State the preparation type.
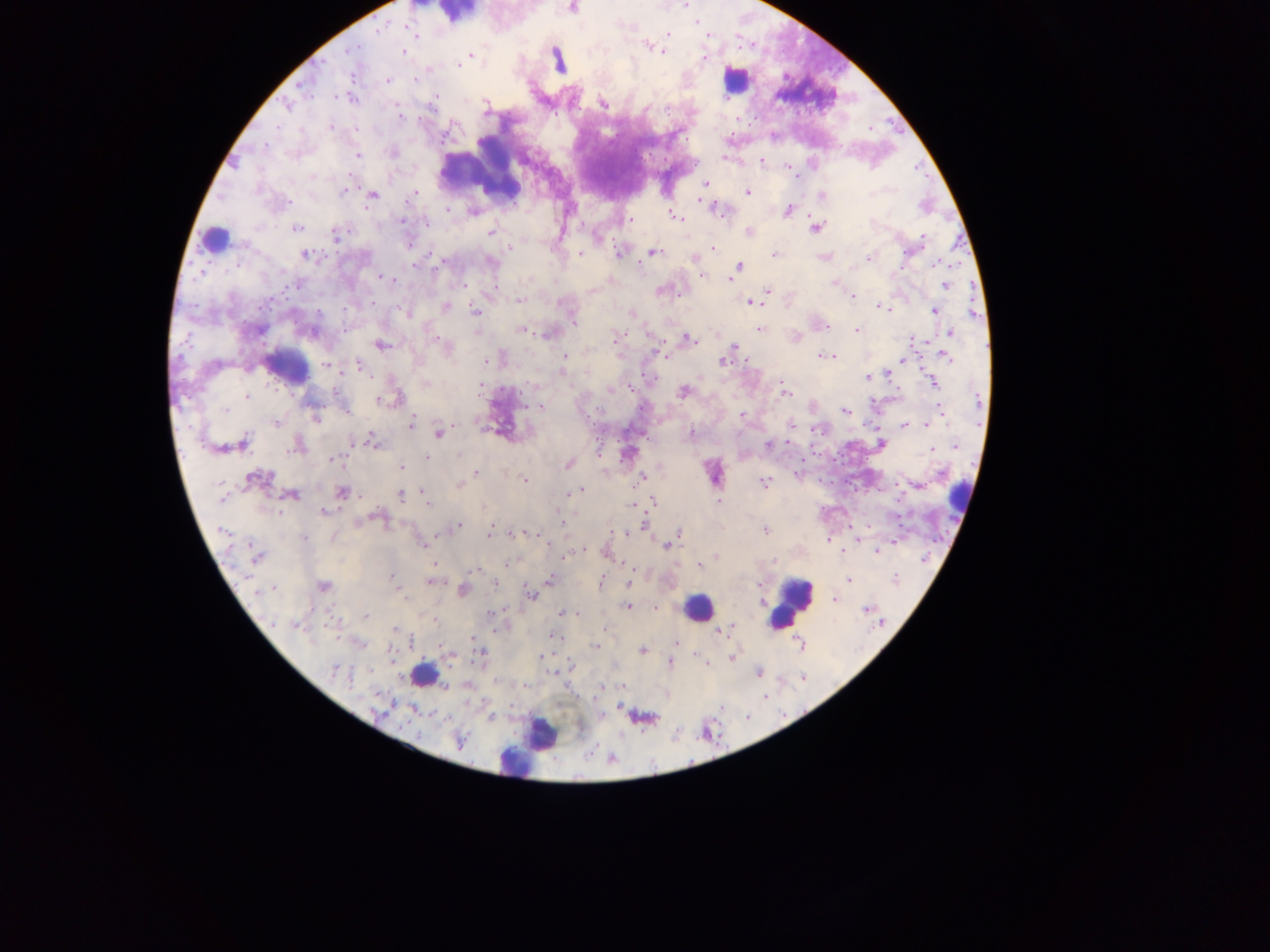

Thick blood film.

image size = 1270×952 pixels
field of view = single
malaria parasite locations = approximate centers as x y in pixels: 571 7; 667 34; 414 35; 708 36; 648 45; 347 50; 662 50; 402 51; 471 55; 703 58; 558 60; 457 65; 387 80; 413 81; 442 94; 602 103; 286 106; 486 106; 402 115; 556 116; 422 119; 330 127; 869 130; 734 132; 391 153; 357 155; 725 157; 759 161; 789 167; 912 169; 930 177; 705 184; 344 189; 747 192; 371 194; 413 195; 822 195; 700 202; 710 206; 715 208; 448 210; 788 210; 473 211; 677 216; 626 219; 401 220; 427 222; 815 226; 297 228; 491 232; 749 232; 336 236; 919 243; 713 248; 509 249; 620 252; 652 252; 580 253; 901 253; 305 255; 774 255; 869 256; 824 257; 694 258; 442 261; 490 262; 935 265; 415 266; 739 266; 901 268; 703 275; 381 278; 390 279; 730 280; 835 282; 292 285; 463 285; 944 285; 661 290; 767 290; 681 296; 852 296; 273 299; 519 301; 750 301; 194 306; 445 307; 879 307; 260 311; 475 312; 934 312; 407 313; 631 313; 573 322; 826 327; 520 329; 758 329; 856 329; 550 333; 950 333; 192 334; 433 337; 795 337; 615 338; 687 339; 924 341; 379 344; 734 346; 656 352; 565 354; 835 354; 832 355; 944 355; 823 356; 901 359; 487 360; 723 360; 746 360; 357 364; 327 365; 887 374; 867 376; 641 377; 783 382; 932 383; 426 384; 609 390; 522 391; 683 391; 783 392; 478 394; 394 397; 378 400; 539 406; 641 409; 846 411; 942 412; 589 415; 316 416; 742 416; 274 422; 410 423; 925 423; 905 425; 789 427; 815 429; 439 432; 692 433; 373 443; 240 444; 769 444; 880 444; 298 445; 956 445; 230 446; 931 449; 598 453; 628 453; 424 456; 839 457; 332 459; 801 459; 568 463; 401 467; 476 472; 797 474; 642 477; 817 478; 256 479; 524 480; 764 484; 836 484; 460 485; 917 485; 581 488; 341 491; 422 491; 290 494; 400 494; 569 494; 652 500; 427 502; 718 502; 633 504; 323 512; 378 517; 562 523; 645 523; 456 526; 869 527; 850 528; 765 530; 677 532; 515 533; 625 533; 487 535; 828 540; 895 541; 549 543; 423 544; 666 545; 876 550; 582 551; 843 551; 606 552; 257 556; 717 556; 562 558; 924 560; 773 561; 506 563; 700 565; 632 569; 473 571; 894 574; 392 576; 848 580; 432 581; 548 581; 630 581; 600 583; 495 584; 323 586; 463 590; 401 593; 531 595; 835 599; 627 606; 654 607; 504 608; 868 609; 560 613; 577 614; 366 616; 296 625; 605 628; 394 630; 719 630; 554 637; 471 638; 799 643; 676 644; 595 646; 441 649; 643 651; 541 655; 696 656; 731 657; 670 663; 337 670; 758 672; 557 675; 493 676; 803 680; 523 685; 620 685; 767 697; 592 700; 723 707; 605 712; 749 717; 458 741; 699 745
country = Ghana
capture = mobile-phone photograph through a microscope
leukocyte locations = approximate centers as x y in pixels: 456 14; 735 80; 211 237; 286 367; 713 472; 958 498; 791 603; 698 607; 422 674; 542 734; 531 745; 514 761